Give the extent of all uninfected red blood cells.
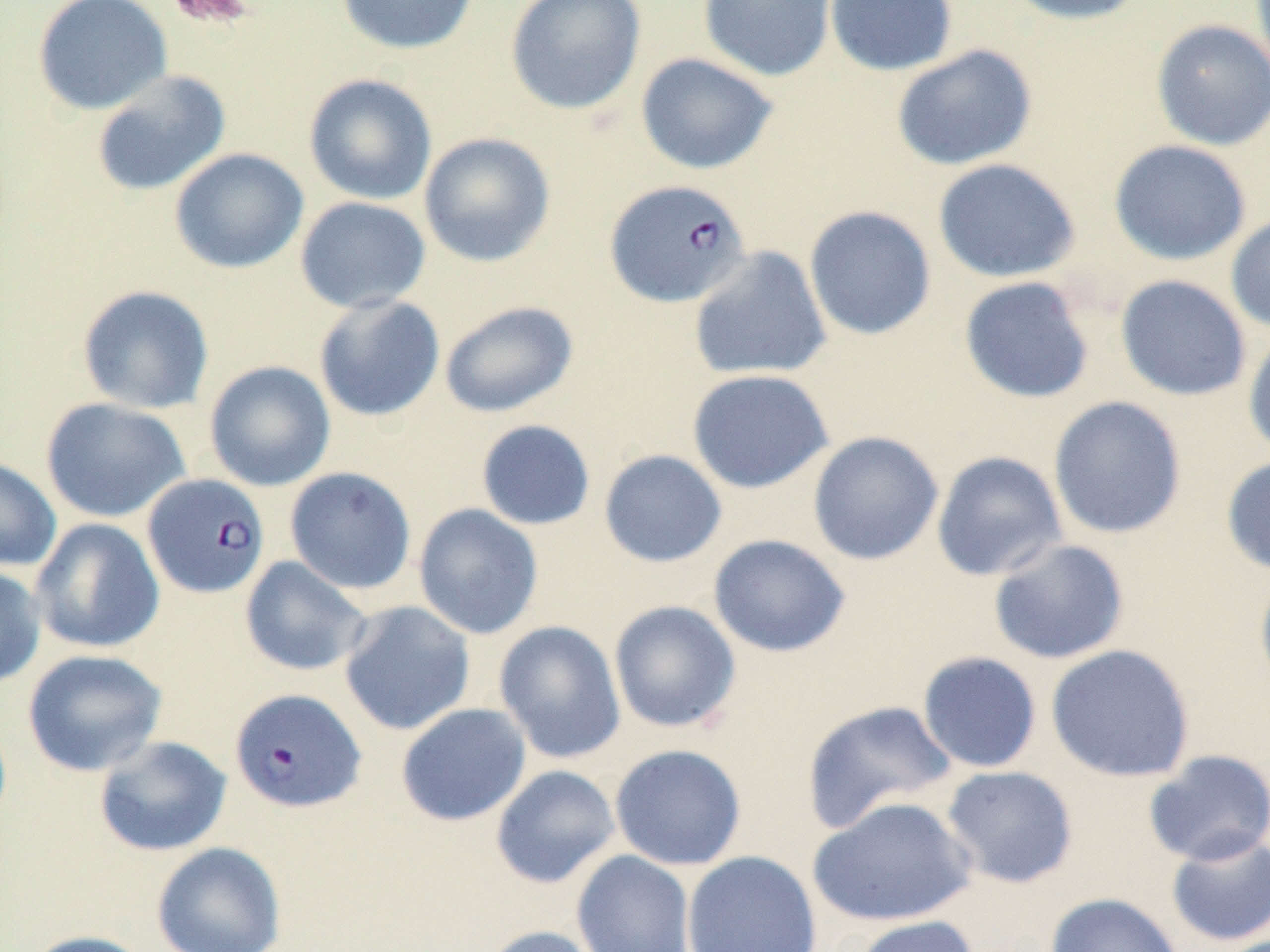
Approximate bounding boxes as named x1/y1/x2/y2 corners in pixels.
Uninfected red blood cells: (x1=32, y1=0, x2=172, y2=115), (x1=335, y1=0, x2=480, y2=55), (x1=505, y1=0, x2=646, y2=116), (x1=697, y1=0, x2=837, y2=82), (x1=824, y1=0, x2=958, y2=76), (x1=1000, y1=0, x2=1150, y2=26), (x1=1151, y1=19, x2=1270, y2=151), (x1=890, y1=44, x2=1038, y2=171), (x1=634, y1=52, x2=779, y2=175), (x1=91, y1=69, x2=231, y2=197), (x1=303, y1=73, x2=437, y2=205), (x1=419, y1=132, x2=555, y2=267), (x1=1108, y1=139, x2=1251, y2=266), (x1=169, y1=147, x2=309, y2=274), (x1=932, y1=158, x2=1081, y2=283), (x1=294, y1=196, x2=431, y2=314), (x1=803, y1=205, x2=937, y2=341), (x1=1225, y1=212, x2=1270, y2=335), (x1=688, y1=245, x2=832, y2=382), (x1=1114, y1=274, x2=1251, y2=401), (x1=958, y1=276, x2=1095, y2=404), (x1=77, y1=284, x2=214, y2=414), (x1=313, y1=294, x2=446, y2=422), (x1=439, y1=300, x2=579, y2=418), (x1=1243, y1=325, x2=1270, y2=461), (x1=204, y1=360, x2=336, y2=492), (x1=686, y1=368, x2=834, y2=494), (x1=1048, y1=396, x2=1186, y2=540), (x1=40, y1=397, x2=190, y2=523), (x1=475, y1=419, x2=596, y2=531), (x1=807, y1=431, x2=944, y2=566), (x1=598, y1=449, x2=727, y2=568), (x1=931, y1=450, x2=1068, y2=582), (x1=1221, y1=454, x2=1270, y2=578), (x1=0, y1=456, x2=62, y2=571), (x1=284, y1=466, x2=417, y2=595), (x1=413, y1=503, x2=544, y2=640), (x1=29, y1=518, x2=165, y2=654), (x1=708, y1=534, x2=851, y2=658), (x1=987, y1=538, x2=1130, y2=665), (x1=239, y1=556, x2=372, y2=677), (x1=0, y1=565, x2=47, y2=688), (x1=1254, y1=565, x2=1270, y2=699), (x1=339, y1=600, x2=476, y2=736), (x1=608, y1=600, x2=742, y2=734), (x1=494, y1=621, x2=626, y2=764), (x1=1045, y1=644, x2=1195, y2=782), (x1=22, y1=648, x2=167, y2=777), (x1=917, y1=651, x2=1042, y2=773), (x1=801, y1=699, x2=958, y2=834), (x1=395, y1=702, x2=531, y2=826), (x1=94, y1=735, x2=232, y2=857), (x1=609, y1=743, x2=746, y2=871), (x1=1142, y1=749, x2=1270, y2=866), (x1=490, y1=765, x2=620, y2=889), (x1=940, y1=765, x2=1079, y2=889), (x1=808, y1=796, x2=978, y2=928), (x1=1165, y1=831, x2=1270, y2=947), (x1=152, y1=842, x2=286, y2=952), (x1=571, y1=849, x2=696, y2=952), (x1=682, y1=850, x2=822, y2=952), (x1=1044, y1=892, x2=1185, y2=952), (x1=851, y1=915, x2=981, y2=952), (x1=478, y1=925, x2=601, y2=952), (x1=20, y1=930, x2=154, y2=952).

Plasmodium falciparum-infected red blood cell locations = approximate bounding boxes as named x1/y1/x2/y2 corners in pixels: (x1=604, y1=179, x2=751, y2=308), (x1=143, y1=473, x2=270, y2=599), (x1=230, y1=687, x2=366, y2=814)
slide-level diagnosis = Plasmodium falciparum
magnification = 1000x
stain = May-Grünwald-Giemsa
modality = optical microscopy
preparation = thin blood film
field of view = one of a larger specimen
image size = 1270×952 pixels
platelet locations = approximate bounding boxes as named x1/y1/x2/y2 corners in pixels: (x1=162, y1=0, x2=260, y2=30)